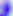
modality = micrograph
identification = Toxoplasma gondii
magnification = 400x